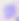
{
  "magnification": "400x",
  "modality": "micrograph",
  "identification": "Toxoplasma gondii"
}